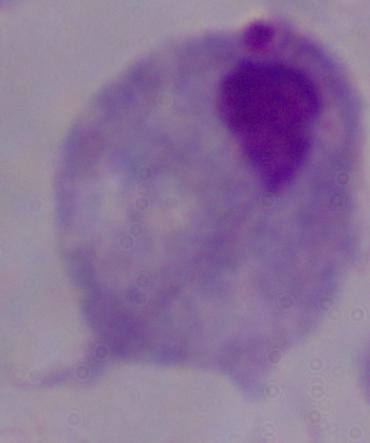

magnification = 1000x
identification = trichomonad
modality = micrograph